Give the extent of all Trypanosoma brucei.
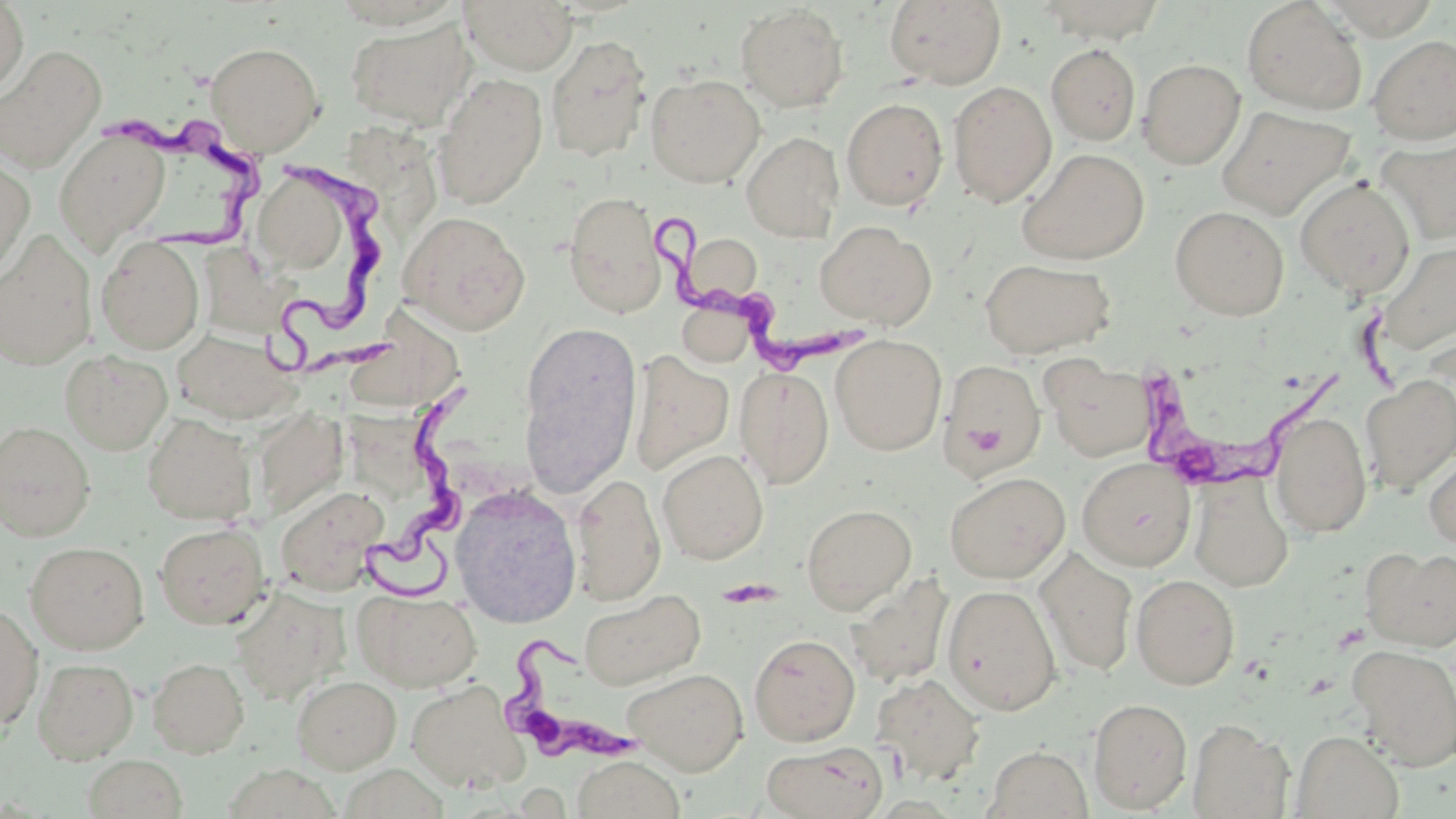
Approximate bounding boxes as (x1, y1, x2, y2) in pixels.
Trypanosoma brucei: (90, 98, 261, 267), (267, 153, 402, 381), (649, 210, 866, 376), (1148, 349, 1338, 494), (350, 387, 481, 601), (493, 628, 645, 772).

Summary:
  - Uninfected red blood cell locations: (0, 0, 28, 97), (459, 0, 578, 74), (885, 0, 1007, 88), (1242, 0, 1367, 114), (1319, 0, 1441, 39), (1037, 1, 1167, 44), (736, 4, 849, 112), (345, 17, 474, 131), (545, 34, 652, 162), (1368, 35, 1456, 144), (205, 41, 324, 155), (1046, 43, 1141, 145), (0, 46, 106, 173), (1045, 48, 1244, 150), (1137, 58, 1246, 169), (433, 73, 548, 209), (645, 73, 765, 187), (948, 80, 1057, 207), (841, 97, 948, 210), (1215, 105, 1355, 220), (54, 128, 170, 251), (742, 131, 843, 242), (1375, 137, 1456, 245), (1017, 148, 1149, 265), (0, 157, 35, 279), (256, 171, 353, 274), (1295, 176, 1416, 297), (563, 191, 667, 318), (1170, 205, 1290, 320), (399, 210, 530, 335), (814, 221, 935, 328), (0, 230, 97, 370), (683, 234, 764, 306), (96, 236, 205, 353), (1376, 240, 1456, 355), (208, 251, 302, 330), (979, 258, 1115, 358), (678, 299, 756, 367), (355, 310, 469, 406), (518, 322, 642, 491), (172, 328, 297, 424), (830, 334, 947, 455), (60, 349, 172, 454), (628, 350, 734, 475), (941, 359, 1045, 480), (1044, 359, 1154, 461), (734, 367, 835, 488), (1361, 375, 1456, 494), (251, 407, 347, 520), (1270, 411, 1372, 539), (143, 413, 257, 525), (355, 413, 433, 490), (0, 420, 96, 541), (1423, 447, 1456, 553), (657, 448, 768, 564), (1078, 457, 1195, 571), (944, 472, 1070, 583), (570, 473, 667, 604), (1189, 473, 1294, 591), (275, 485, 389, 595), (451, 485, 582, 627), (801, 503, 917, 613), (154, 522, 270, 629), (25, 541, 149, 654), (1361, 545, 1456, 652), (1036, 549, 1138, 676), (846, 573, 954, 688), (1131, 573, 1240, 690), (943, 584, 1062, 715), (230, 585, 348, 705), (354, 590, 481, 691), (579, 590, 706, 690), (0, 603, 43, 731), (749, 634, 860, 746), (1349, 644, 1456, 771), (32, 657, 138, 764), (147, 657, 249, 758), (622, 667, 748, 774), (870, 673, 986, 784), (292, 674, 401, 773), (406, 680, 526, 791), (1088, 697, 1193, 813), (1187, 719, 1293, 818), (1293, 730, 1404, 819), (761, 740, 889, 819), (984, 746, 1093, 819), (82, 754, 187, 818), (572, 756, 685, 819)
  - Slide-level diagnosis: Trypanosoma brucei
  - Stain: May-Grünwald-Giemsa
  - Modality: optical microscopy
  - Field of view: one of a larger specimen
  - Magnification: 1000x
  - Preparation: thin blood film
  - Image size: 1456×819 pixels